Give the position of every Plasmodium parasite.
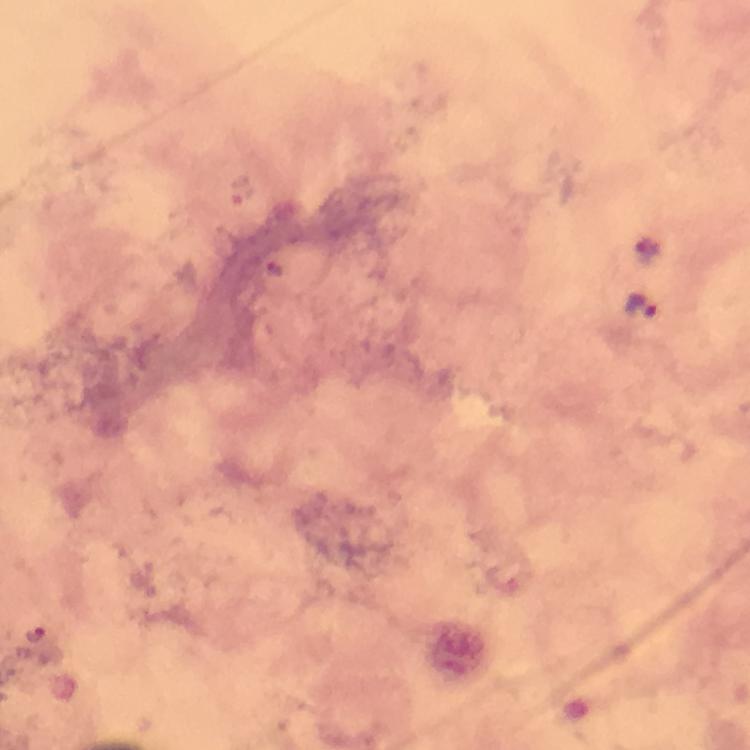

Approximate object centers, in pixels from the top-left corner.
Plasmodium parasites: (x=642, y=307), (x=38, y=634).

100x magnification. Image is 750×750 pixels. Photographed through the microscope with a smartphone camera. Cropped region of a single field of view. From a malaria diagnostic workup. Immersion oil was used. Thick blood film. Giemsa-stained preparation.